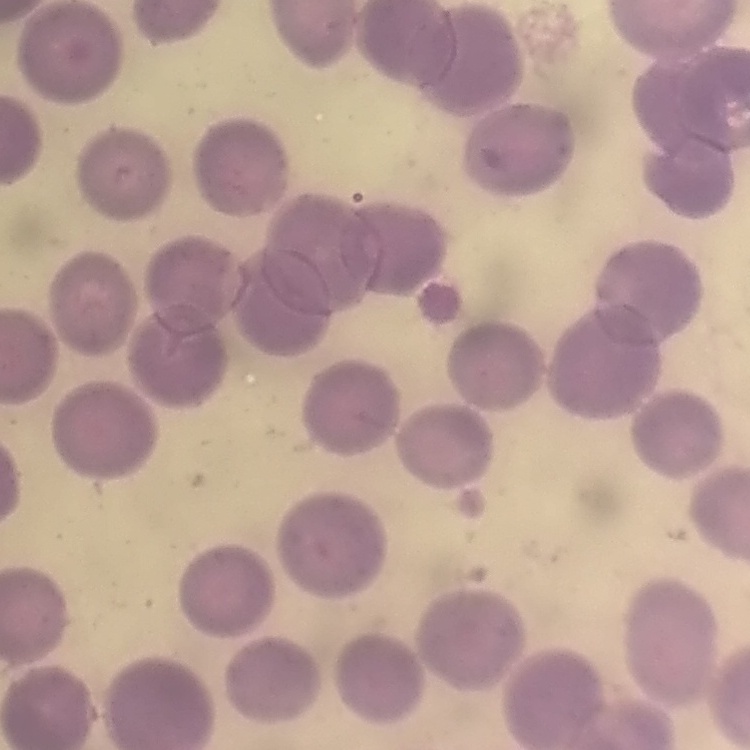

erythrocyte_morphology: no rouleaux formation
image_type: square crop of a larger photomicrograph
preparation: thin peripheral smear
stain: Field's or Giemsa